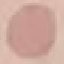

Result: negative for malaria parasites. Giemsa-stained preparation. Photographed with a smartphone camera at the microscope eyepiece. Cell patch, automatically extracted from a larger field of view and resized to 64 × 64 pixels. Thin blood film.